Outline each Plasmodium malariae-infected red blood cell.
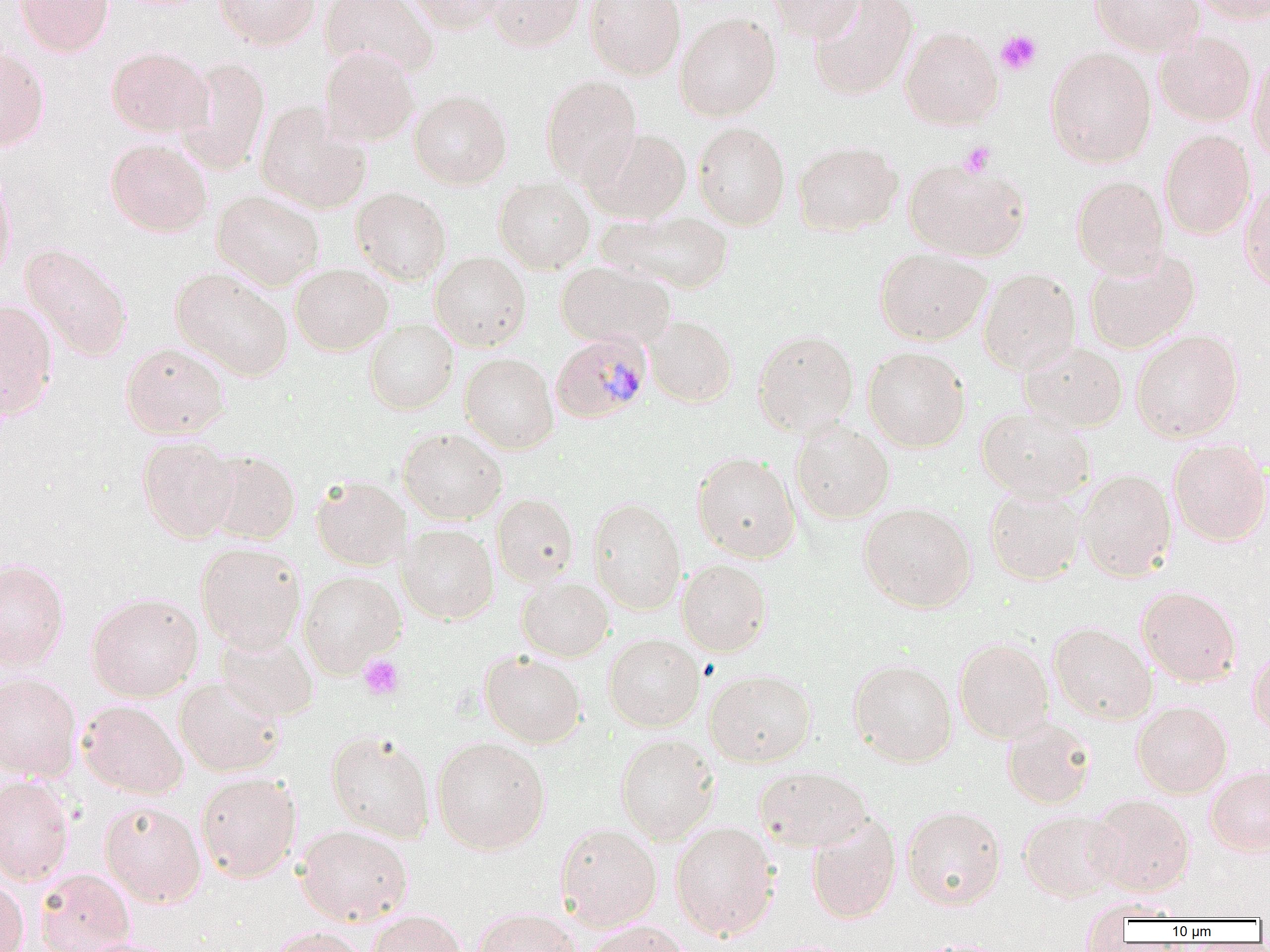

Approximate bounding boxes as [x1, y1, x2, y2] in pixels.
Plasmodium malariae-infected red blood cells: [550, 332, 653, 423].

slide-level diagnosis = Plasmodium malariae
preparation = thin blood smear
image size = 1270×952 pixels
uninfected red blood cell locations = approximate bounding boxes as [x1, y1, x2, y2] in pixels: [15, 0, 114, 57], [214, 0, 320, 49], [320, 0, 439, 77], [405, 0, 507, 33], [485, 0, 586, 51], [586, 0, 686, 80], [769, 0, 864, 42], [808, 0, 919, 100], [1088, 0, 1205, 56], [1191, 0, 1270, 23], [675, 12, 782, 121], [900, 26, 1003, 129], [1154, 30, 1256, 127], [320, 45, 419, 147], [0, 46, 50, 151], [106, 46, 214, 138], [1045, 47, 1156, 168], [1248, 51, 1270, 163], [177, 57, 270, 174], [541, 75, 642, 187], [409, 89, 512, 189], [256, 102, 372, 214], [692, 121, 790, 231], [588, 127, 692, 223], [1160, 130, 1256, 239], [106, 138, 212, 237], [793, 140, 902, 236], [904, 158, 1031, 261], [0, 165, 16, 284], [1072, 176, 1169, 277], [494, 178, 595, 274], [1240, 179, 1270, 292], [351, 187, 452, 285], [213, 190, 324, 290], [599, 208, 733, 293], [20, 243, 133, 363], [875, 247, 991, 345], [1084, 247, 1200, 354], [871, 249, 981, 451], [430, 251, 531, 350], [556, 260, 675, 349], [290, 264, 393, 355], [170, 266, 293, 382], [978, 267, 1081, 375], [0, 299, 58, 419], [645, 316, 737, 407], [364, 319, 459, 414], [752, 329, 859, 436], [1132, 329, 1244, 442], [120, 342, 230, 439], [1019, 342, 1128, 432], [863, 346, 971, 452], [460, 352, 559, 454], [976, 406, 1095, 502], [791, 419, 894, 523], [398, 426, 507, 525], [137, 435, 240, 543], [1168, 439, 1270, 546], [203, 449, 301, 544], [692, 451, 801, 563], [1077, 469, 1177, 581], [311, 475, 410, 570], [984, 485, 1086, 585], [492, 493, 579, 587], [587, 497, 687, 615], [859, 502, 977, 612], [399, 524, 499, 624], [196, 543, 306, 652], [0, 559, 70, 671], [676, 559, 773, 656], [298, 570, 405, 677], [517, 576, 614, 661], [1136, 585, 1242, 687], [86, 592, 203, 702], [1048, 623, 1156, 725], [214, 629, 319, 721], [604, 633, 705, 731], [954, 638, 1054, 742], [1248, 646, 1270, 737], [480, 650, 586, 748], [849, 659, 957, 766], [705, 669, 816, 767], [0, 671, 82, 781], [174, 675, 286, 777], [78, 700, 188, 799], [1132, 701, 1232, 797], [1002, 717, 1096, 808], [326, 730, 436, 842], [615, 733, 719, 844], [432, 737, 550, 854], [1205, 765, 1270, 856], [755, 766, 872, 852], [196, 772, 301, 882], [0, 774, 75, 885], [1088, 794, 1196, 896], [99, 800, 206, 907], [901, 804, 1007, 909], [1019, 809, 1122, 902], [806, 813, 901, 923], [671, 821, 780, 940], [556, 823, 662, 930], [295, 824, 413, 925], [35, 868, 135, 952], [0, 876, 29, 952], [473, 907, 581, 952], [368, 909, 468, 952], [579, 921, 693, 952], [268, 927, 366, 952], [73, 936, 179, 952], [909, 938, 1008, 952]
platelet locations = approximate bounding boxes as [x1, y1, x2, y2] in pixels: [995, 30, 1042, 75], [959, 141, 995, 176], [359, 655, 404, 699]
magnification = 1000x
field of view = single
modality = light microscopy